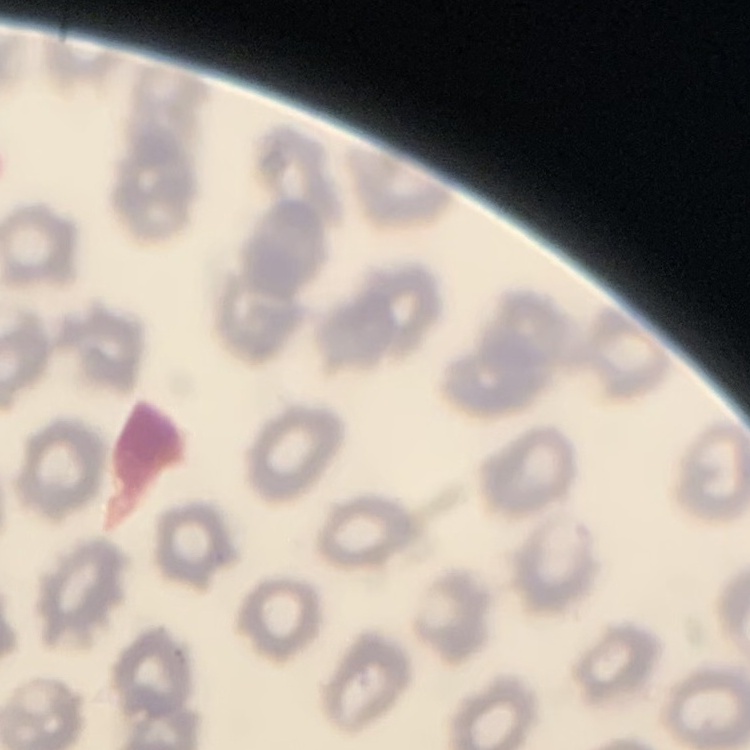 The erythrocytes show no rouleaux formation. One tile cut from a larger photomicrograph. Stained with either Field's or Giemsa. Thin blood film.